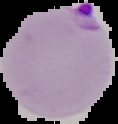

Segmented cell region on a black background. Image is 118×124 pixels. Result: malaria parasites detected. From a thin blood smear.